Describe the morphology of the erythrocytes.
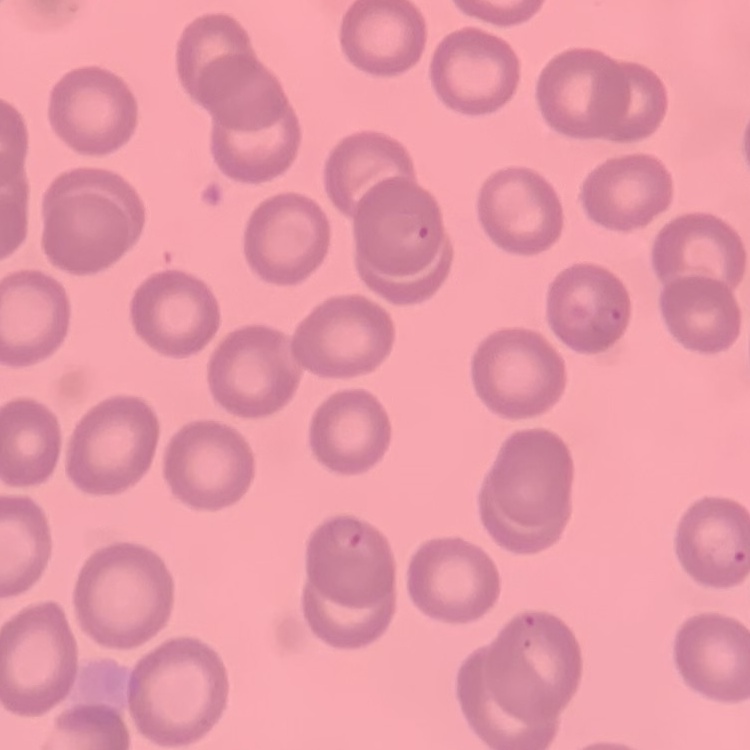

They show no rouleaux formation.

Summary:
  - Stain: Field's or Giemsa
  - Image type: square crop of a larger photomicrograph
  - Preparation: thin peripheral smear